Locate every uninfected red blood cell.
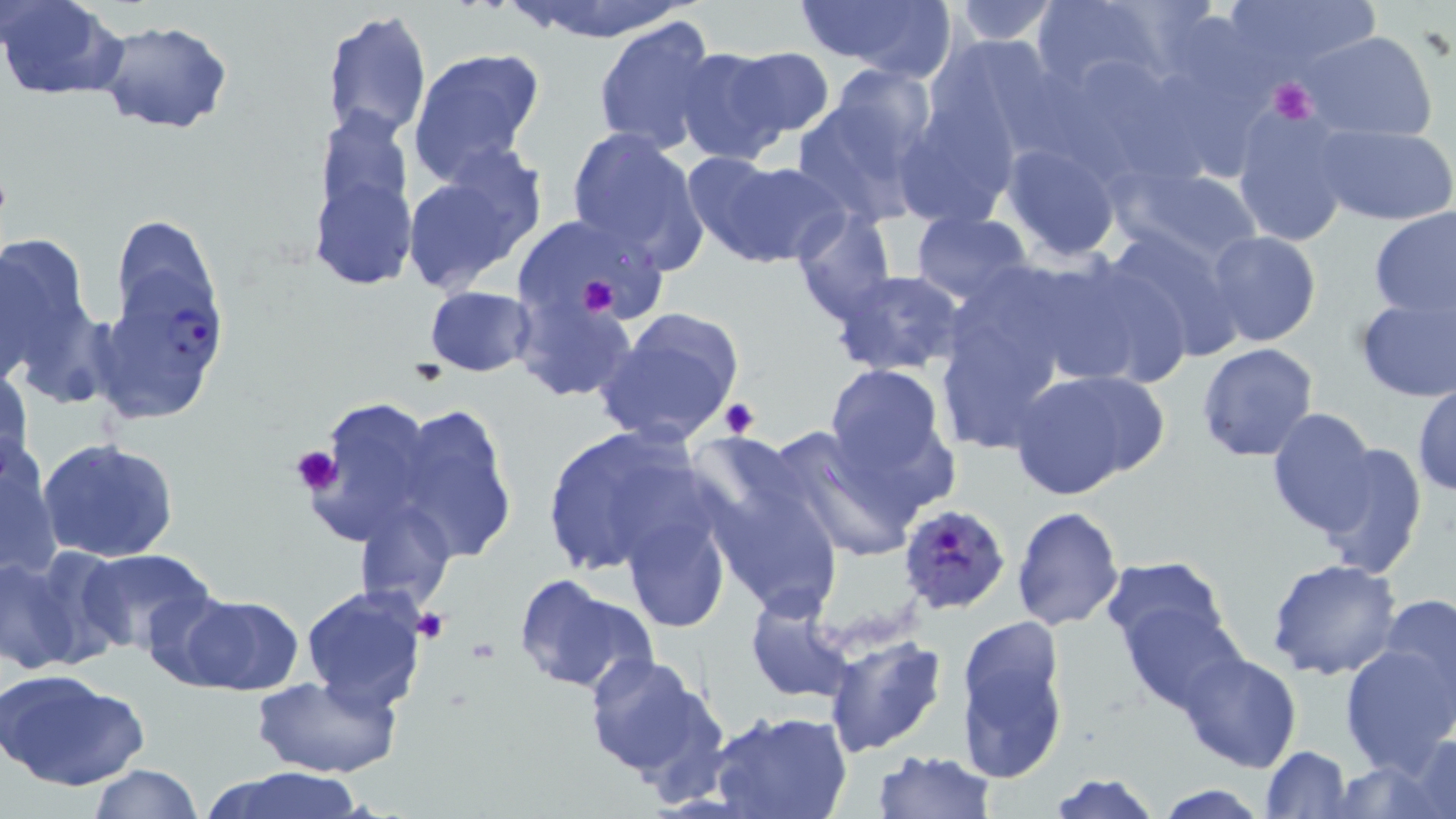
Approximate bounding boxes as [x1, y1, x2, y2] in pixels.
Uninfected red blood cells: [0, 0, 129, 101], [508, 0, 700, 44], [796, 0, 958, 81], [949, 0, 1060, 47], [1030, 0, 1172, 95], [1219, 0, 1384, 79], [323, 9, 432, 142], [592, 16, 721, 159], [97, 21, 233, 134], [1304, 31, 1438, 142], [924, 33, 1063, 157], [406, 47, 546, 185], [728, 47, 833, 138], [674, 48, 794, 165], [1040, 51, 1206, 183], [824, 66, 937, 166], [792, 91, 933, 227], [892, 101, 1018, 230], [313, 106, 414, 244], [1230, 106, 1354, 246], [1318, 124, 1456, 226], [565, 126, 707, 271], [1001, 141, 1123, 263], [400, 149, 547, 297], [689, 155, 847, 269], [1123, 164, 1264, 265], [312, 173, 416, 291], [1368, 207, 1455, 320], [790, 209, 896, 324], [910, 210, 1035, 305], [1101, 225, 1244, 363], [0, 230, 103, 398], [1204, 230, 1321, 348], [1032, 254, 1196, 391], [828, 270, 971, 378], [937, 273, 1079, 414], [424, 287, 536, 376], [1355, 292, 1456, 403], [511, 294, 635, 403], [595, 307, 746, 446], [98, 326, 209, 426], [1196, 340, 1321, 462], [823, 363, 953, 494], [1, 368, 31, 480], [1008, 370, 1161, 502], [1412, 382, 1456, 496], [304, 396, 438, 551], [393, 401, 518, 564], [1266, 408, 1382, 538], [537, 423, 717, 581], [776, 423, 937, 559], [38, 439, 179, 564], [1313, 441, 1430, 576], [0, 442, 63, 581], [695, 453, 845, 618], [356, 501, 454, 610], [1010, 506, 1125, 630], [623, 509, 733, 635], [75, 548, 222, 659], [1099, 555, 1232, 661], [1266, 557, 1403, 681], [0, 558, 83, 675], [513, 573, 659, 696], [300, 586, 429, 713], [1377, 591, 1456, 720], [173, 593, 305, 697], [745, 594, 856, 704], [1121, 604, 1248, 715], [953, 617, 1072, 781], [823, 635, 948, 758], [1339, 640, 1455, 776], [582, 649, 727, 790], [1177, 649, 1303, 771], [0, 668, 149, 791], [252, 674, 401, 779], [709, 711, 851, 819], [1404, 730, 1456, 816], [1260, 746, 1352, 818], [872, 748, 996, 819], [1326, 759, 1451, 817], [89, 764, 203, 819], [206, 766, 366, 819], [1047, 773, 1164, 819], [1152, 784, 1270, 818].

Plasmodium falciparum-infected red blood cell locations: [111, 277, 239, 383], [900, 503, 1011, 614]. Platelet locations: [1267, 77, 1317, 123], [574, 274, 621, 318], [719, 398, 761, 439], [290, 445, 342, 495], [415, 607, 450, 642], [465, 637, 503, 664]. Slide-level diagnosis: Plasmodium falciparum. Thin blood smear. One field of a larger specimen. 1000x magnification. Image is 1456×819 pixels. Optical microscopy. May-Grünwald-Giemsa-stained preparation.